Assess this cell for malaria.
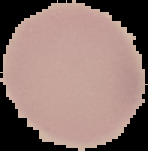

It is uninfected.

image type = segmented cell region on a black background
image size = 148×151 pixels
preparation = thin blood film